Assess this cell for malaria.
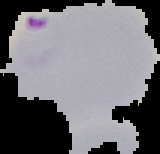

It is parasitized.

Summary:
  - Image type: cell region segmented out of the field of view; surrounding area masked to black
  - Preparation: thin blood film
  - Image size: 160×154 pixels